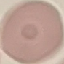
Malaria status: uninfected. Acquired by smartphone through the microscope eyepiece. Automatically extracted cell patch, resized to 64 × 64 pixels. Giemsa stain. Thin blood film.